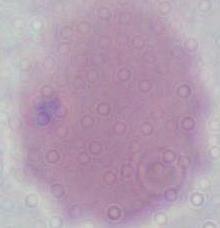
An erythrocyte is shown. 1000x magnification. Micrograph.